State the blood parasite species.
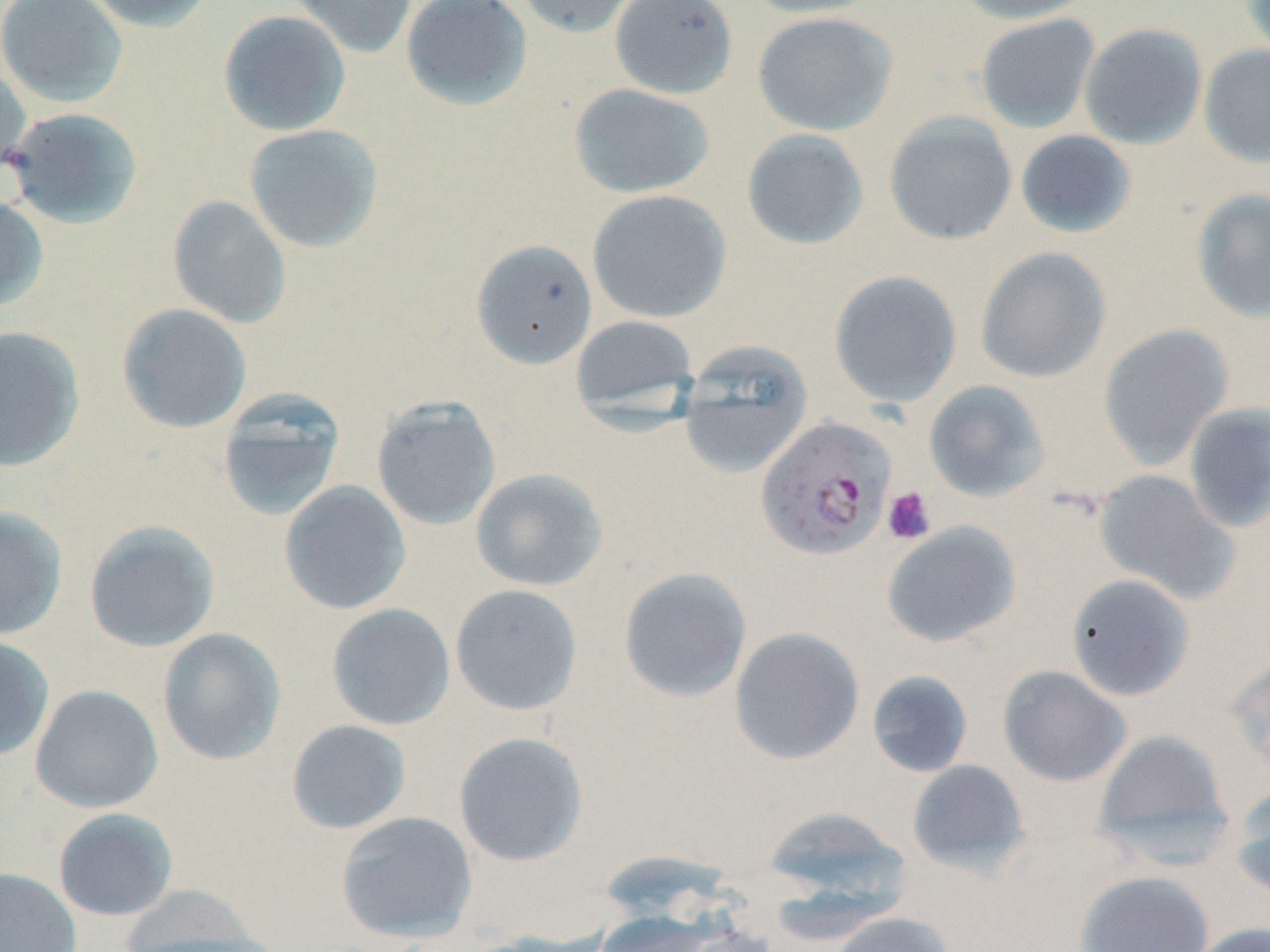

Plasmodium falciparum.

Approximate bounding boxes as (x1,y1)-(x2,y2) corner pairs in pixels. Platelet locations: (882,486)-(937,545). Plasmodium falciparum-infected red blood cell locations: (755,416)-(896,560). Uninfected red blood cell locations: (0,0)-(128,108), (84,0)-(217,33), (287,0)-(417,59), (401,0)-(533,111), (511,0)-(641,38), (609,0)-(739,99), (743,0)-(884,19), (952,0)-(1096,25), (1238,0)-(1270,61), (218,9)-(352,137), (751,11)-(898,136), (975,14)-(1101,133), (1079,23)-(1207,149), (1199,44)-(1270,168), (0,62)-(31,184), (567,83)-(714,199), (4,107)-(144,229), (882,112)-(1017,246), (243,124)-(384,253), (741,128)-(869,250), (1015,130)-(1137,239), (1190,187)-(1270,324), (587,189)-(732,323), (0,194)-(49,312), (167,195)-(292,329), (471,239)-(598,369), (975,246)-(1112,383), (828,270)-(962,408), (117,303)-(252,433), (569,314)-(700,423), (1098,324)-(1234,469), (0,325)-(85,472), (679,344)-(813,479), (923,380)-(1050,503), (216,390)-(346,522), (371,395)-(501,530), (1182,401)-(1270,533), (470,468)-(608,592), (1093,470)-(1240,604), (278,480)-(411,615), (0,506)-(68,640), (83,519)-(221,653), (881,521)-(1021,648), (618,567)-(753,703), (1066,574)-(1196,701), (449,584)-(583,715), (326,603)-(456,730), (728,626)-(864,764), (157,627)-(287,765), (0,635)-(55,762), (1226,655)-(1270,776), (998,665)-(1132,788), (866,670)-(974,778), (30,684)-(164,813), (286,719)-(412,834), (1092,728)-(1236,866), (453,732)-(588,866), (906,759)-(1031,877), (1231,782)-(1270,905), (761,804)-(910,910), (52,807)-(179,921), (335,810)-(478,942), (0,867)-(82,952), (1074,870)-(1215,952), (116,884)-(274,950), (590,910)-(719,952), (827,911)-(954,952), (1188,922)-(1270,952). 1000x magnification. Light microscopy. Single field of view. Image is 1270×952 pixels. May-Grünwald-Giemsa stain. Thin blood smear.